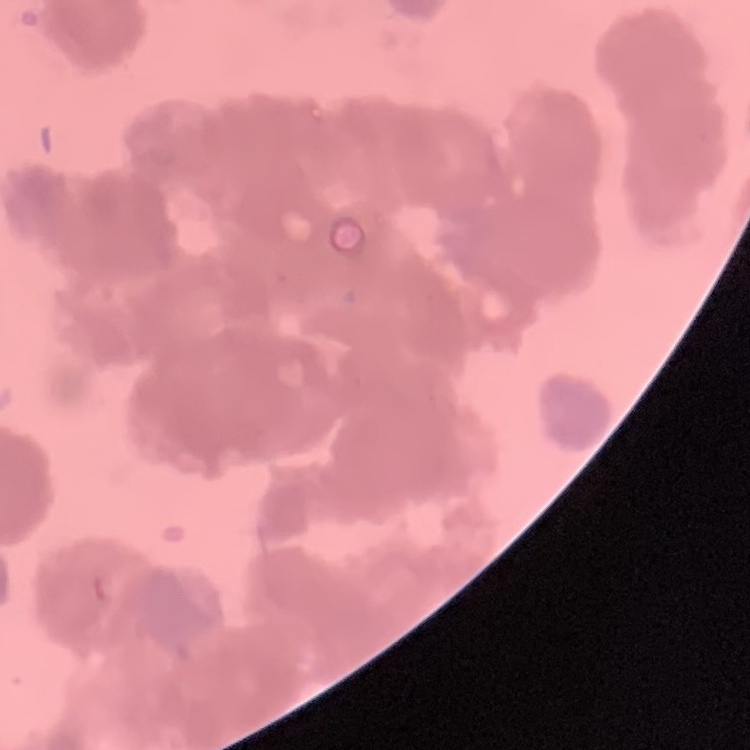

Summary:
  - Erythrocyte morphology: rouleaux formation
  - Image type: one tile cut from a larger photomicrograph
  - Stain: Field's or Giemsa
  - Preparation: thin blood smear